State which parasite is depicted.
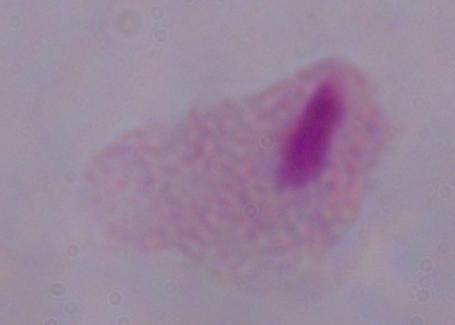
A trichomonad.

{
  "modality": "micrograph",
  "magnification": "1000x"
}